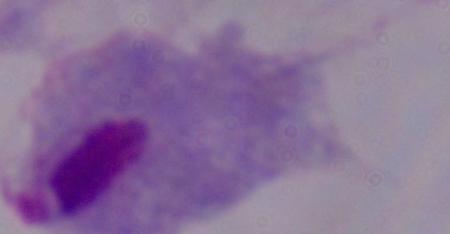

identification = trichomonad
modality = photomicrograph
magnification = 1000x